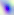 Captured at 400x magnification. Photomicrograph. Toxoplasma gondii is seen.